Identify the cell.
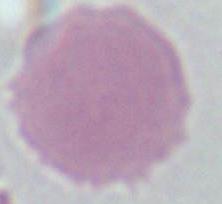
This is an erythrocyte.

Summary:
  - Magnification: 1000x
  - Modality: micrograph